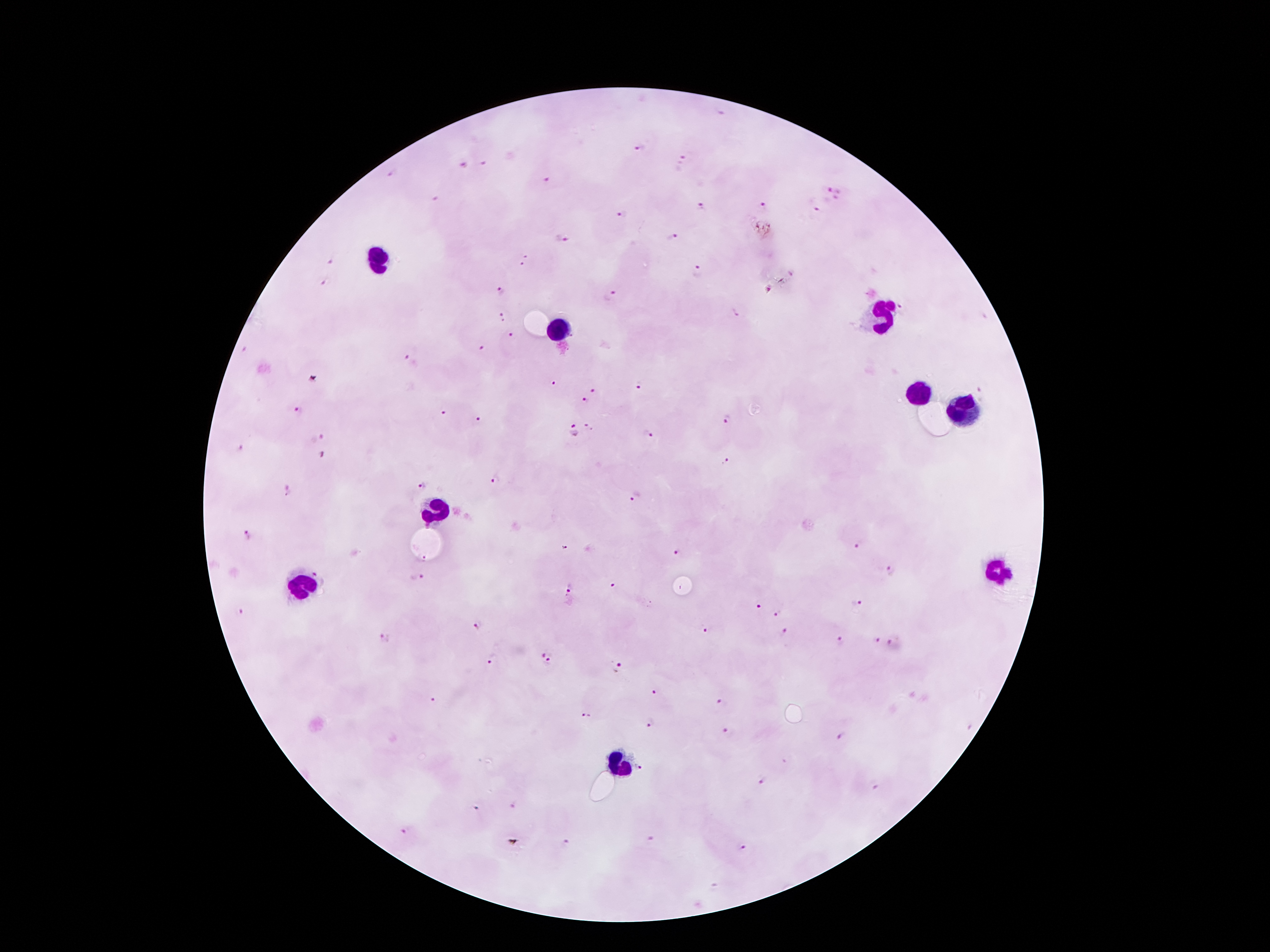
Approximate object centers, in pixels from the top-left corner. Leukocyte locations: (x=373, y=257), (x=884, y=311), (x=560, y=332), (x=915, y=395), (x=961, y=406), (x=438, y=510), (x=995, y=572), (x=295, y=584), (x=617, y=763). Malaria parasite locations: (x=641, y=149), (x=683, y=158), (x=483, y=161), (x=464, y=164), (x=391, y=173), (x=547, y=180), (x=834, y=190), (x=437, y=201), (x=703, y=207), (x=764, y=207), (x=817, y=211), (x=623, y=216), (x=562, y=238), (x=672, y=238), (x=529, y=255), (x=332, y=261), (x=522, y=265), (x=697, y=273), (x=324, y=281), (x=767, y=288), (x=502, y=291), (x=611, y=296), (x=902, y=307), (x=735, y=311), (x=502, y=315), (x=510, y=334), (x=482, y=348), (x=408, y=359), (x=553, y=383), (x=639, y=386), (x=591, y=391), (x=982, y=391), (x=586, y=400), (x=300, y=410), (x=443, y=413), (x=478, y=419), (x=728, y=422), (x=589, y=427), (x=573, y=432), (x=647, y=434), (x=315, y=438), (x=241, y=450), (x=325, y=454), (x=725, y=461), (x=495, y=480), (x=422, y=485), (x=288, y=491), (x=636, y=499), (x=248, y=535), (x=859, y=546), (x=679, y=556), (x=891, y=570), (x=417, y=579), (x=613, y=586), (x=568, y=589), (x=856, y=604), (x=758, y=606), (x=777, y=610), (x=239, y=613), (x=476, y=626), (x=708, y=631), (x=784, y=635), (x=876, y=640), (x=385, y=641), (x=840, y=642), (x=892, y=644), (x=547, y=651), (x=494, y=661), (x=549, y=664), (x=618, y=668), (x=657, y=692), (x=435, y=700), (x=720, y=703), (x=588, y=715), (x=651, y=723), (x=727, y=730), (x=841, y=738), (x=643, y=768), (x=761, y=782), (x=876, y=788), (x=515, y=807), (x=475, y=810), (x=407, y=832), (x=650, y=839), (x=565, y=843), (x=742, y=848), (x=713, y=887). Image is 1270×952 pixels. 100x magnification. Thick blood smear. Single field of view. Smartphone photograph taken through the microscope eyepiece. Patient malaria status: positive for Plasmodium falciparum. Giemsa-stained preparation.